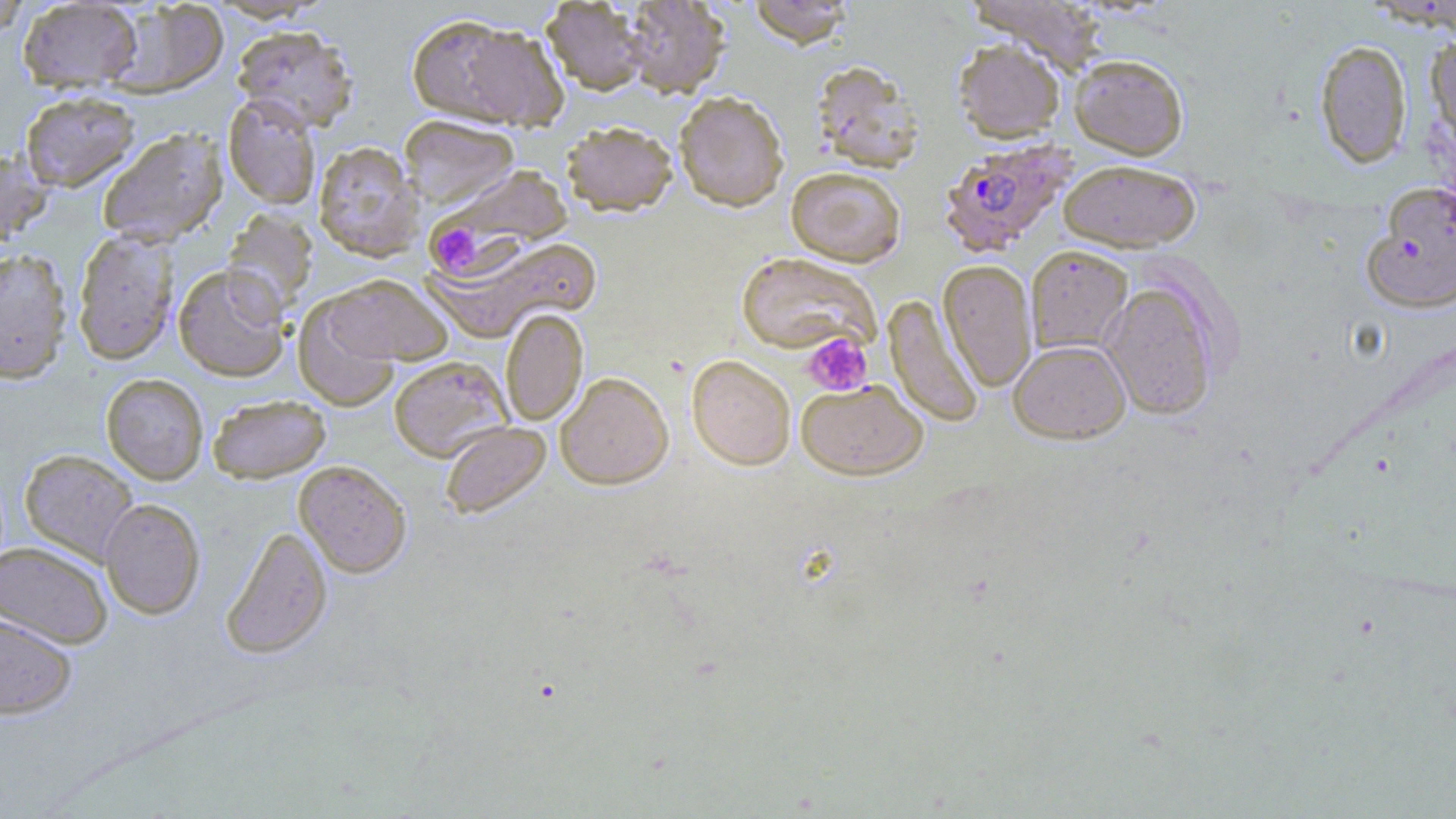
Approximate bounding boxes as [x1, y1, x2, y2] in pixels. Uninfected red blood cell locations: [0, 0, 31, 39], [17, 0, 143, 93], [620, 0, 730, 98], [747, 0, 854, 47], [967, 0, 1109, 74], [106, 1, 229, 97], [542, 1, 650, 95], [408, 16, 566, 129], [232, 24, 358, 132], [1425, 34, 1456, 142], [953, 38, 1066, 143], [1314, 39, 1412, 168], [1070, 53, 1188, 159], [811, 60, 923, 173], [20, 90, 140, 191], [674, 90, 789, 211], [223, 94, 321, 209], [399, 115, 520, 208], [561, 121, 678, 215], [97, 129, 228, 247], [313, 141, 423, 262], [0, 147, 51, 250], [1058, 158, 1201, 252], [786, 167, 906, 266], [421, 168, 576, 277], [1363, 182, 1456, 313], [222, 208, 319, 314], [72, 227, 179, 365], [430, 234, 605, 341], [75, 243, 289, 372], [1026, 245, 1133, 355], [0, 248, 73, 383], [736, 251, 881, 356], [939, 259, 1037, 392], [173, 264, 291, 382], [325, 274, 453, 365], [1101, 281, 1219, 420], [293, 295, 401, 410], [884, 295, 983, 428], [500, 308, 588, 426], [1009, 339, 1130, 444], [687, 355, 796, 470], [388, 356, 512, 462], [555, 371, 673, 490], [101, 373, 208, 485], [796, 379, 927, 480], [207, 394, 331, 483], [440, 422, 550, 519], [19, 449, 139, 565], [294, 460, 412, 578], [100, 498, 205, 619], [220, 524, 332, 659], [0, 540, 113, 648], [0, 612, 77, 719]. Plasmodium falciparum-infected red blood cell locations: [938, 138, 1076, 257]. Platelet locations: [437, 227, 477, 269], [802, 333, 873, 395]. Slide-level diagnosis: Plasmodium falciparum. Captured at 1000x magnification. One field of a larger specimen. Thin blood film. Image is 1456×819 pixels. May-Grünwald-Giemsa stain. Optical microscopy.